Locate every leukocyte (white blood cell).
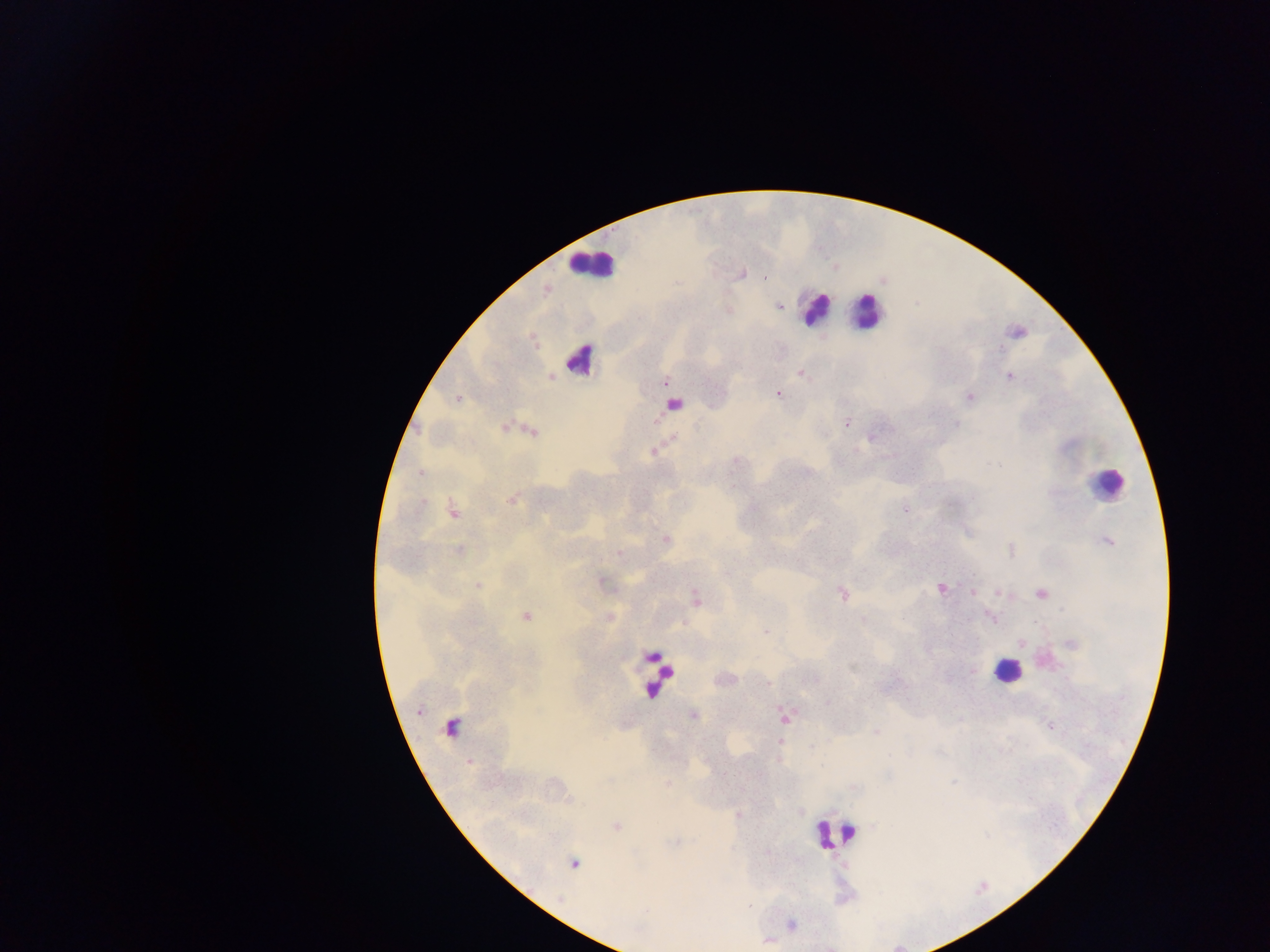
Approximate centers as {x, y} in pixels.
Leukocytes: {591, 265}, {813, 309}, {865, 312}, {581, 360}, {675, 404}, {1106, 484}, {1006, 671}, {662, 672}, {832, 833}.

Plasmodium parasite locations: {743, 273}, {763, 277}, {779, 306}, {1000, 349}, {801, 373}, {1009, 376}, {665, 382}, {777, 393}, {457, 398}, {970, 398}, {846, 424}, {955, 424}, {504, 428}, {532, 432}, {653, 452}, {421, 473}, {512, 500}, {422, 501}, {905, 509}, {453, 511}, {666, 540}, {1107, 542}, {459, 550}, {1010, 551}, {618, 553}, {478, 585}, {940, 589}, {973, 593}, {999, 593}, {843, 594}, {1041, 594}, {526, 617}, {766, 632}, {1072, 643}, {1021, 644}, {972, 671}, {769, 683}, {693, 715}, {1049, 726}, {451, 727}, {876, 732}, {779, 742}, {469, 762}, {668, 784}, {616, 826}, {574, 864}, {749, 906}. Collected in Ghana. Thick blood film. One field of view. Image is 1270×952 pixels. Photographed through a microscope with a mobile-phone camera.